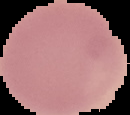

Summary:
  - Preparation: thin blood film
  - Image type: segmented cell region on a black background
  - Malaria status: uninfected
  - Image size: 130×115 pixels